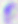

{
  "modality": "photomicrograph",
  "identification": "Toxoplasma gondii",
  "magnification": "400x"
}